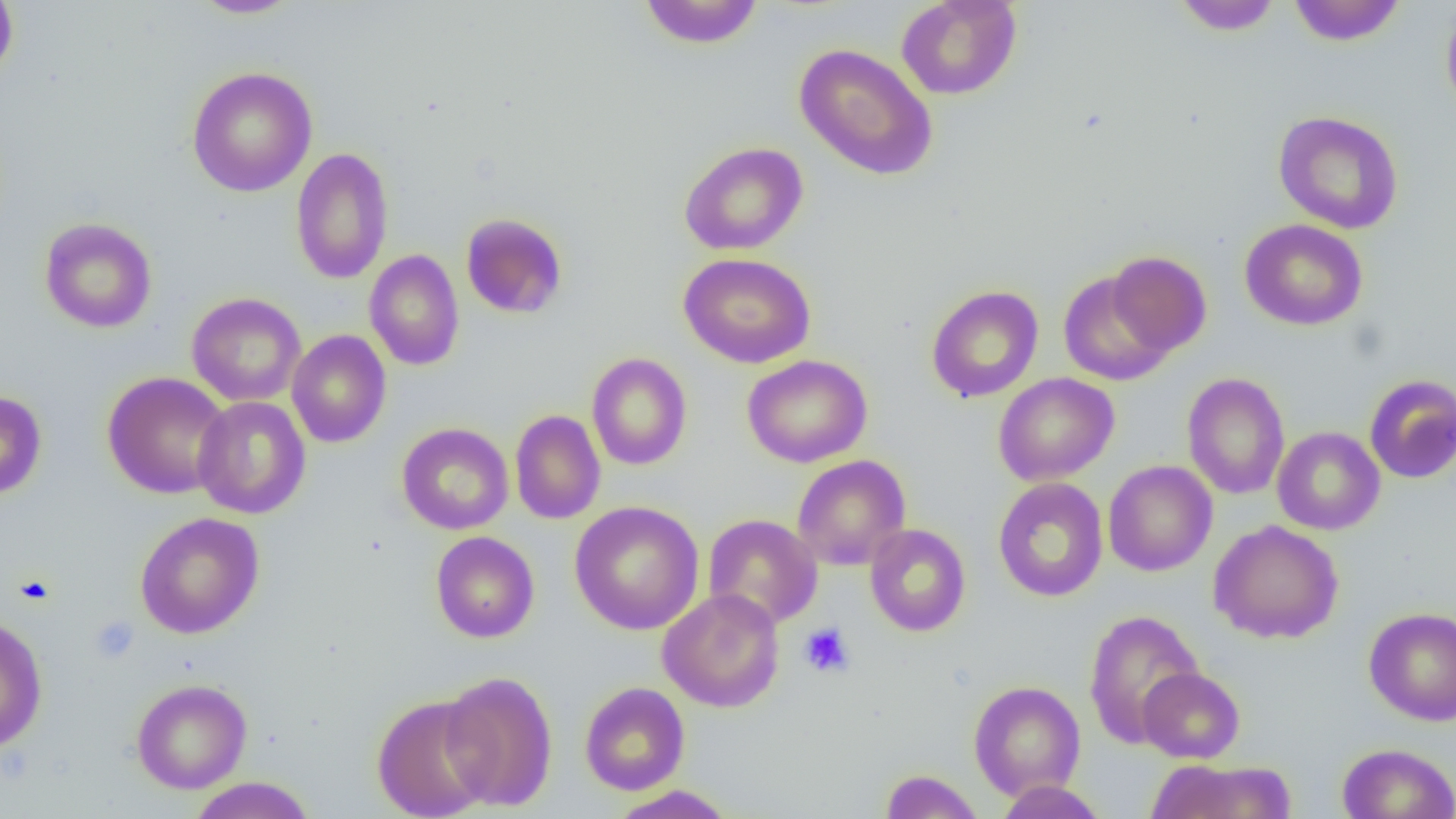
Summary:
  - Coordinate format: approximate bounding boxes as named x1/y1/x2/y2 corners in pixels
  - Uninfected red blood cell locations: (x1=0, y1=0, x2=18, y2=84), (x1=190, y1=0, x2=301, y2=19), (x1=638, y1=0, x2=763, y2=49), (x1=895, y1=0, x2=1022, y2=100), (x1=1172, y1=0, x2=1283, y2=35), (x1=1287, y1=0, x2=1406, y2=46), (x1=1441, y1=1, x2=1456, y2=120), (x1=794, y1=43, x2=940, y2=181), (x1=187, y1=66, x2=318, y2=197), (x1=1273, y1=110, x2=1404, y2=234), (x1=679, y1=141, x2=809, y2=255), (x1=290, y1=147, x2=394, y2=285), (x1=460, y1=212, x2=568, y2=319), (x1=39, y1=217, x2=157, y2=333), (x1=1240, y1=219, x2=1368, y2=331), (x1=364, y1=249, x2=465, y2=371), (x1=1105, y1=251, x2=1212, y2=356), (x1=678, y1=252, x2=816, y2=369), (x1=1058, y1=271, x2=1174, y2=386), (x1=925, y1=284, x2=1044, y2=402), (x1=186, y1=292, x2=306, y2=406), (x1=286, y1=330, x2=392, y2=448), (x1=586, y1=352, x2=692, y2=470), (x1=742, y1=354, x2=873, y2=467), (x1=102, y1=371, x2=232, y2=499), (x1=993, y1=372, x2=1120, y2=486), (x1=1182, y1=372, x2=1290, y2=500), (x1=1364, y1=374, x2=1456, y2=483), (x1=0, y1=390, x2=47, y2=500), (x1=193, y1=396, x2=311, y2=519), (x1=510, y1=410, x2=606, y2=524), (x1=397, y1=422, x2=514, y2=535), (x1=1271, y1=426, x2=1385, y2=535), (x1=792, y1=454, x2=911, y2=571), (x1=1103, y1=460, x2=1217, y2=576), (x1=992, y1=477, x2=1108, y2=602), (x1=569, y1=501, x2=705, y2=635), (x1=135, y1=512, x2=265, y2=639), (x1=703, y1=514, x2=822, y2=629), (x1=1208, y1=520, x2=1345, y2=644), (x1=865, y1=523, x2=971, y2=637), (x1=431, y1=531, x2=540, y2=643), (x1=658, y1=588, x2=785, y2=712), (x1=1363, y1=607, x2=1456, y2=726), (x1=1083, y1=609, x2=1205, y2=748), (x1=0, y1=617, x2=48, y2=753), (x1=1138, y1=668, x2=1245, y2=763), (x1=439, y1=670, x2=558, y2=811), (x1=131, y1=679, x2=252, y2=793), (x1=969, y1=680, x2=1085, y2=800), (x1=579, y1=682, x2=690, y2=795), (x1=372, y1=694, x2=495, y2=819), (x1=1337, y1=742, x2=1455, y2=819), (x1=1145, y1=758, x2=1297, y2=818), (x1=879, y1=769, x2=984, y2=818), (x1=187, y1=777, x2=317, y2=819), (x1=995, y1=780, x2=1109, y2=818), (x1=608, y1=785, x2=737, y2=818)
  - Platelet locations: (x1=13, y1=573, x2=57, y2=607), (x1=89, y1=616, x2=139, y2=663), (x1=799, y1=623, x2=854, y2=678)
  - Slide-level diagnosis: no evidence of blood parasites
  - Field of view: single
  - Preparation: thin blood film
  - Magnification: 1000x
  - Modality: optical microscopy
  - Image size: 1456×819 pixels